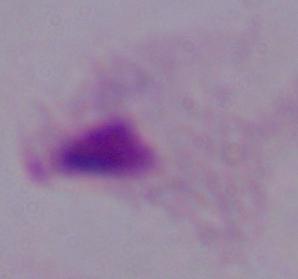
{
  "modality": "micrograph",
  "identification": "trichomonad",
  "magnification": "1000x"
}